Comment on the morphology of the erythrocytes.
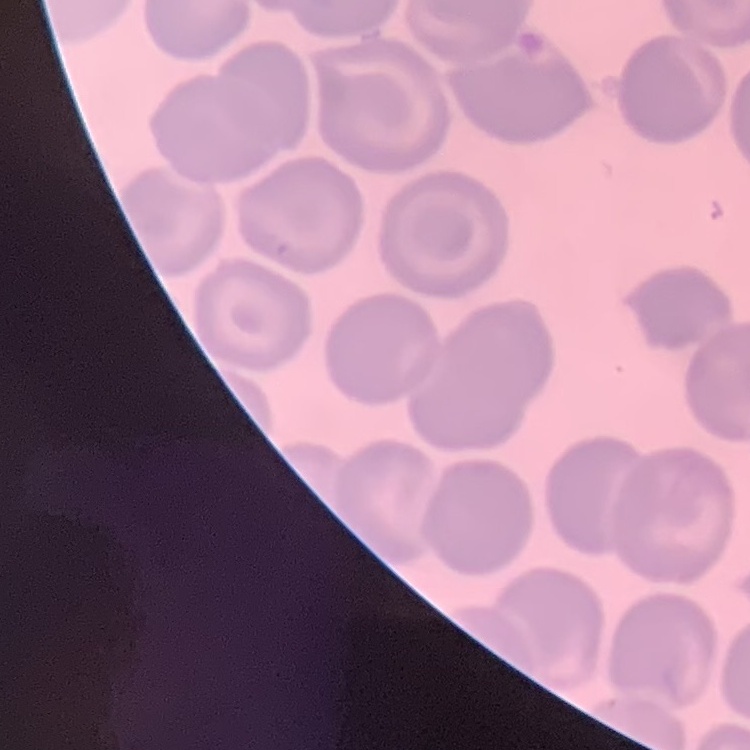
They show no rouleaux formation.

Stained with either Field's or Giemsa. Square crop of a larger photomicrograph. Thin peripheral smear.